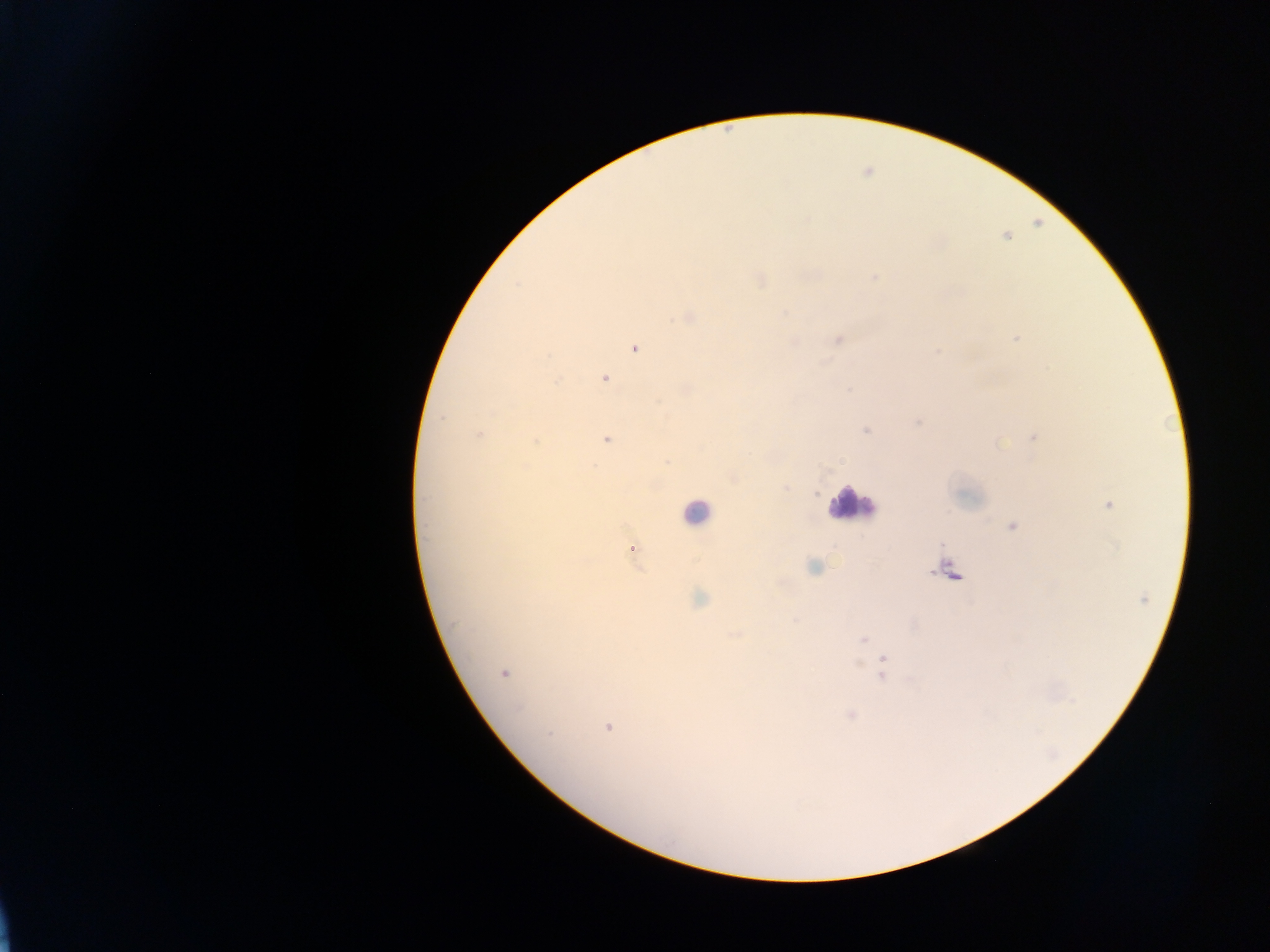 Approximate centers as [x, y] in pixels. Leukocyte locations: [851, 504], [696, 511], [949, 571]. Malaria parasite locations: [873, 278], [759, 279], [687, 317], [838, 338], [1017, 338], [635, 347], [604, 377], [916, 422], [867, 430], [479, 434], [1034, 437], [606, 438], [535, 440], [784, 487], [1107, 503], [1012, 526], [630, 548], [814, 567], [698, 599], [863, 638], [883, 660], [502, 672], [883, 676], [851, 715], [607, 726]. Collected in Ghana. Mobile-phone photograph taken through the microscope. Single field of view. Image is 1270×952 pixels. Thick blood smear.